Classify this cell by malaria status.
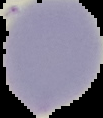

Uninfected.

image size = 103×118 pixels
preparation = thin blood film
image type = segmented cell region with the area outside set to black